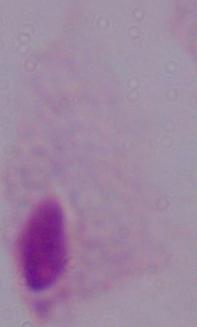
Summary:
  - Magnification: 1000x
  - Modality: micrograph
  - Identification: trichomonad